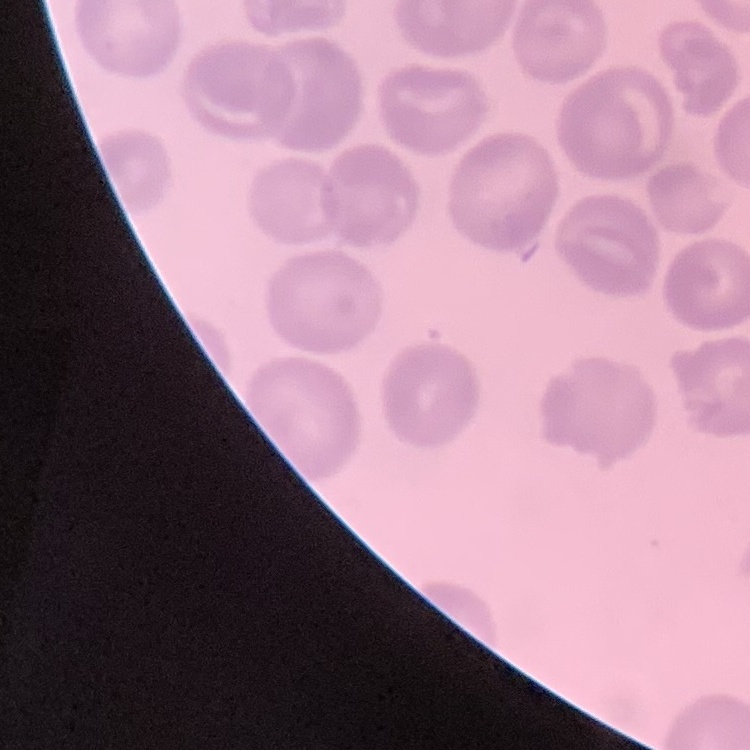
The red blood cells show no rouleaux formation. Thin blood film. Square crop of a larger photomicrograph. Stained with either Field's or Giemsa.